Give the extent of all uninfected red blood cells.
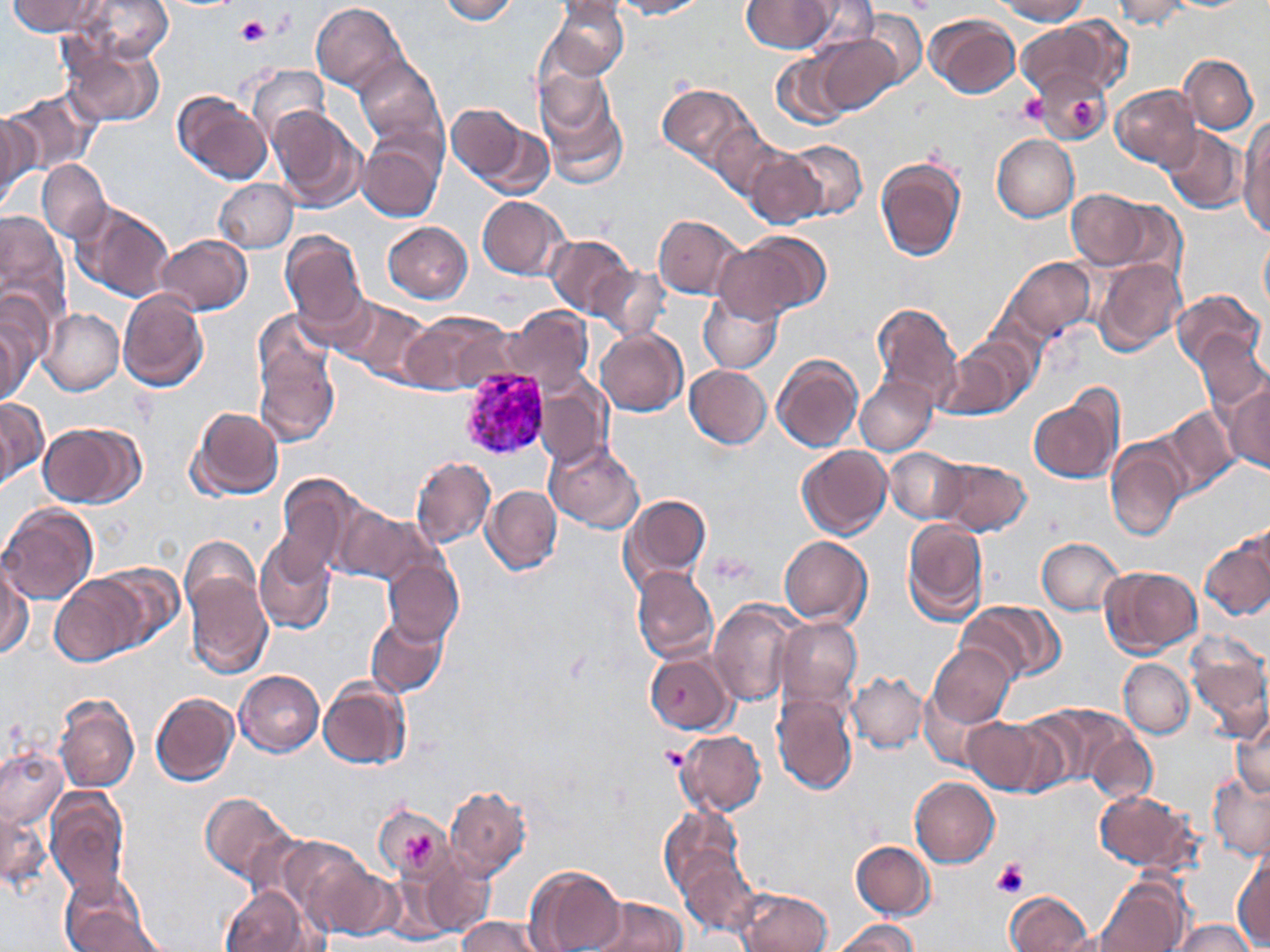

Approximate bounding boxes as (x1,y1)-(x2,y2) corner pairs in pixels.
Uninfected red blood cells: (78,0)-(175,64), (437,0)-(521,25), (610,0)-(706,18), (795,0)-(881,50), (991,0)-(1091,23), (1112,0)-(1194,31), (8,1)-(102,36), (312,1)-(408,95), (546,1)-(629,80), (741,1)-(836,54), (860,9)-(928,90), (927,12)-(1021,99), (1017,19)-(1126,101), (811,34)-(903,117), (61,39)-(167,127), (772,48)-(851,127), (354,52)-(447,153), (1181,54)-(1257,133), (247,63)-(332,145), (534,65)-(629,189), (1035,71)-(1113,146), (657,85)-(755,172), (1111,85)-(1201,169), (6,88)-(99,179), (173,91)-(272,185), (445,101)-(544,193), (264,102)-(365,214), (0,109)-(42,210), (708,119)-(792,206), (1237,119)-(1270,235), (1160,125)-(1245,214), (357,129)-(446,224), (992,134)-(1079,222), (783,139)-(867,221), (745,148)-(824,230), (876,155)-(967,262), (36,159)-(111,242), (214,178)-(298,254), (1067,189)-(1153,269), (477,196)-(568,279), (70,201)-(176,303), (0,208)-(69,336), (653,214)-(746,299), (382,221)-(473,303), (716,231)-(826,324), (280,232)-(369,336), (157,234)-(251,313), (547,234)-(634,317), (1259,234)-(1270,315), (1003,256)-(1096,342), (1094,259)-(1186,354), (593,264)-(669,341), (698,287)-(784,373), (117,288)-(210,392), (1172,288)-(1264,373), (0,292)-(49,402), (335,295)-(434,387), (871,302)-(963,408), (39,307)-(123,395), (506,307)-(594,398), (401,312)-(515,397), (250,317)-(341,447), (0,319)-(28,406), (596,329)-(688,416), (1197,331)-(1269,413), (935,349)-(1021,419), (772,353)-(863,452), (685,365)-(772,449), (855,377)-(936,455), (1226,377)-(1269,473), (534,380)-(610,472), (1029,387)-(1124,484), (0,397)-(48,490), (187,405)-(284,499), (1158,407)-(1240,499), (36,423)-(138,507), (1105,439)-(1187,540), (547,440)-(645,532), (797,445)-(893,539), (885,446)-(967,522), (411,456)-(496,547), (934,458)-(1031,536), (276,470)-(373,578), (482,485)-(562,576), (618,493)-(713,595), (0,503)-(98,603), (332,505)-(437,587), (902,518)-(988,625), (1201,529)-(1270,623), (255,535)-(336,635), (779,536)-(872,625), (1036,536)-(1126,615), (180,549)-(275,680), (0,557)-(32,661), (381,559)-(464,646), (629,566)-(720,665), (1098,566)-(1202,659), (49,575)-(145,666), (625,575)-(794,679), (708,601)-(800,705), (957,601)-(1063,686), (365,615)-(448,696), (776,618)-(862,709), (1185,641)-(1270,742), (928,643)-(1015,727), (644,650)-(736,735), (1120,659)-(1193,738), (848,669)-(927,753), (235,670)-(324,756), (319,677)-(412,770), (918,685)-(999,772), (773,690)-(859,795), (56,693)-(139,792), (150,693)-(239,785), (1020,701)-(1135,794), (1232,713)-(1270,800), (965,717)-(1049,795), (675,730)-(767,814), (1091,734)-(1156,804), (0,746)-(68,829), (1206,773)-(1270,861), (909,776)-(1001,868), (445,784)-(531,880), (44,786)-(131,899), (1093,789)-(1202,875), (200,790)-(298,886), (0,797)-(48,890), (374,804)-(451,881), (659,805)-(744,893), (277,834)-(388,935), (851,840)-(935,919), (678,849)-(761,939), (1232,849)-(1268,948), (421,851)-(497,939), (524,864)-(624,952), (57,874)-(159,952), (1093,874)-(1188,952), (219,886)-(315,952), (734,888)-(832,952), (1001,891)-(1094,952), (586,897)-(690,951), (456,916)-(544,952), (831,919)-(920,952), (1170,919)-(1260,952).

slide-level diagnosis = Plasmodium vivax
preparation = thin blood smear
Plasmodium vivax-infected red blood cell locations = approximate bounding boxes as (x1,y1)-(x2,y2) corner pairs in pixels: (458,366)-(549,461)
modality = optical microscopy
magnification = 1000x
field of view = single
stain = May-Grünwald-Giemsa
platelet locations = approximate bounding boxes as (x1,y1)-(x2,y2) corner pairs in pixels: (237,18)-(269,44), (1019,92)-(1049,124), (1070,98)-(1096,128), (711,554)-(756,587), (662,744)-(689,769), (404,835)-(433,869), (993,861)-(1029,898)
image size = 1270×952 pixels